State the blood parasite species.
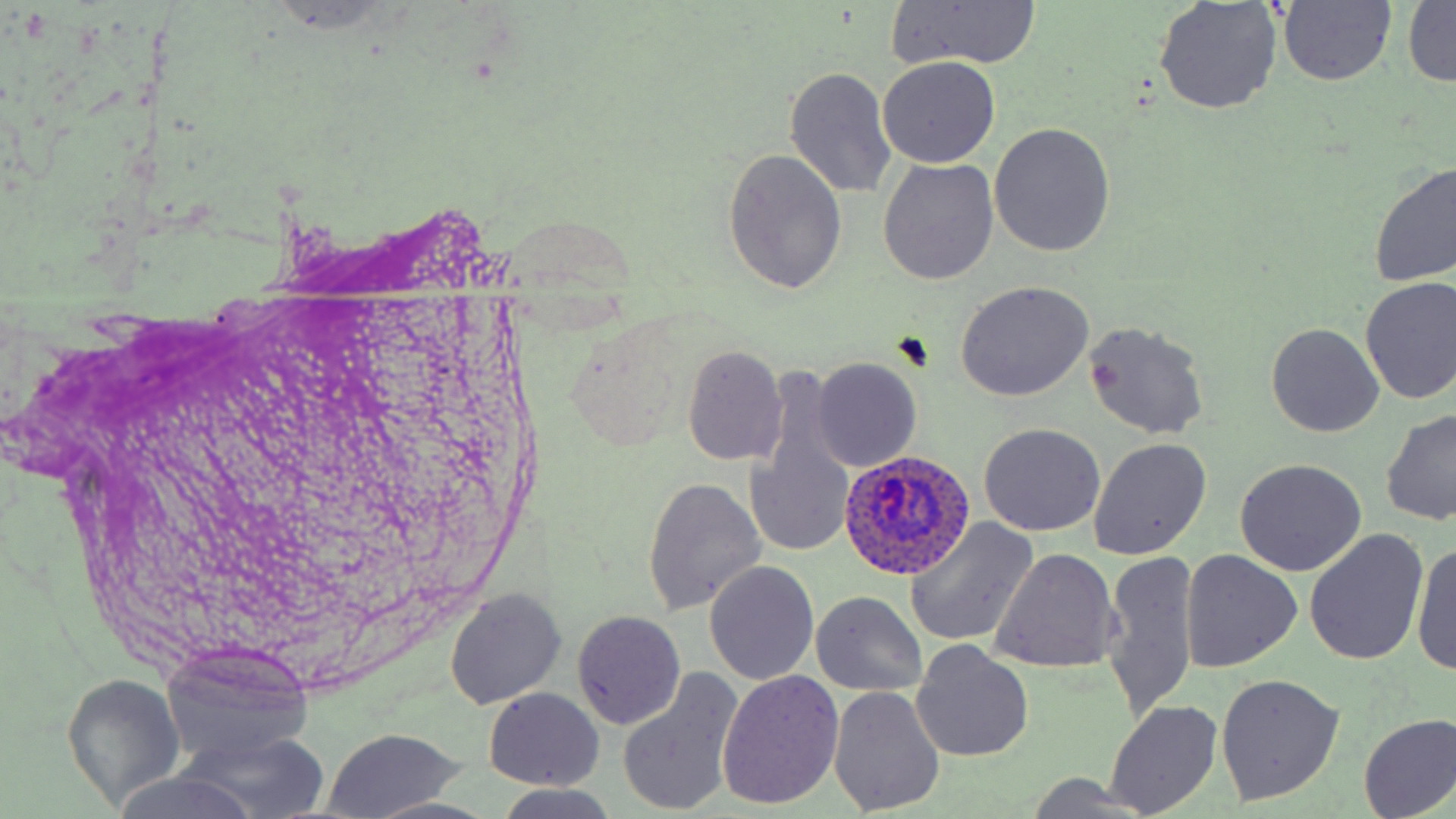
Plasmodium ovale.

magnification = 1000x
modality = light microscopy
field of view = one of a larger specimen
image size = 1456×819 pixels
uninfected red blood cell locations = approximate bounding boxes as named x1/y1/x2/y2 corners in pixels: (x1=1276, y1=1, x2=1396, y2=88), (x1=885, y1=2, x2=1044, y2=71), (x1=1404, y1=2, x2=1456, y2=88), (x1=1153, y1=4, x2=1283, y2=116), (x1=877, y1=56, x2=1001, y2=168), (x1=783, y1=68, x2=898, y2=199), (x1=989, y1=122, x2=1117, y2=257), (x1=722, y1=147, x2=848, y2=295), (x1=877, y1=157, x2=998, y2=286), (x1=1369, y1=161, x2=1456, y2=289), (x1=1358, y1=276, x2=1455, y2=405), (x1=955, y1=280, x2=1095, y2=401), (x1=1082, y1=321, x2=1208, y2=441), (x1=1266, y1=323, x2=1384, y2=438), (x1=682, y1=345, x2=786, y2=464), (x1=811, y1=358, x2=921, y2=471), (x1=745, y1=377, x2=859, y2=565), (x1=1380, y1=410, x2=1456, y2=528), (x1=978, y1=423, x2=1107, y2=536), (x1=1089, y1=438, x2=1212, y2=561), (x1=1234, y1=458, x2=1367, y2=577), (x1=642, y1=476, x2=766, y2=617), (x1=904, y1=518, x2=1039, y2=646), (x1=1304, y1=528, x2=1429, y2=667), (x1=1411, y1=541, x2=1456, y2=677), (x1=991, y1=549, x2=1120, y2=674), (x1=1102, y1=549, x2=1199, y2=722), (x1=1180, y1=550, x2=1302, y2=673), (x1=704, y1=560, x2=819, y2=685), (x1=447, y1=589, x2=564, y2=709), (x1=811, y1=590, x2=927, y2=697), (x1=572, y1=610, x2=686, y2=729), (x1=911, y1=639, x2=1035, y2=762), (x1=169, y1=656, x2=321, y2=812), (x1=616, y1=669, x2=744, y2=818), (x1=719, y1=670, x2=845, y2=809), (x1=1214, y1=673, x2=1344, y2=806), (x1=62, y1=675, x2=185, y2=809), (x1=829, y1=687, x2=945, y2=816), (x1=485, y1=689, x2=603, y2=790), (x1=1106, y1=700, x2=1222, y2=816), (x1=1356, y1=713, x2=1456, y2=819), (x1=319, y1=727, x2=467, y2=819), (x1=178, y1=735, x2=332, y2=819), (x1=109, y1=770, x2=272, y2=819), (x1=493, y1=785, x2=624, y2=818), (x1=369, y1=796, x2=495, y2=818)
Plasmodium ovale-infected red blood cell locations = approximate bounding boxes as named x1/y1/x2/y2 corners in pixels: (x1=836, y1=451, x2=975, y2=579)
preparation = thin blood smear
stain = May-Grünwald-Giemsa